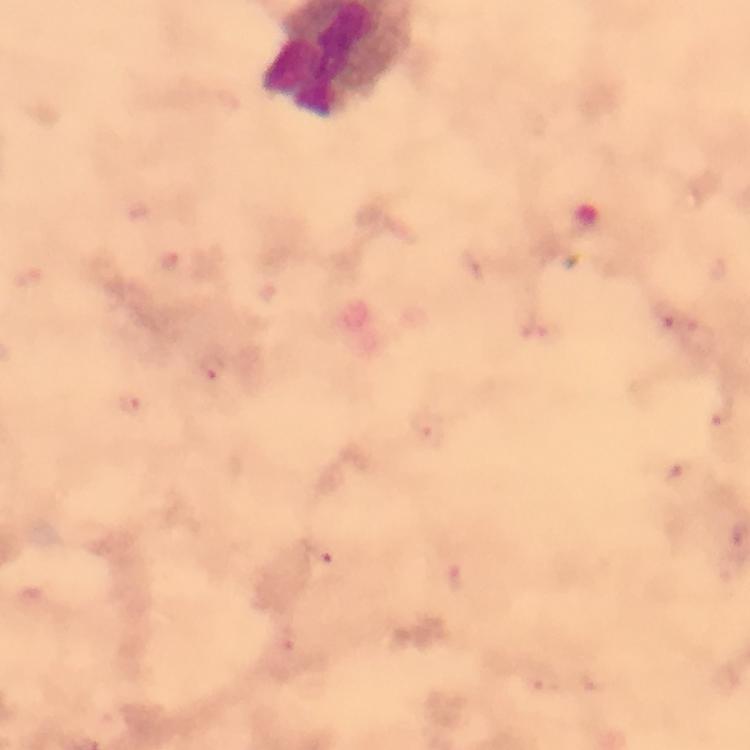
Approximate centers as {x, y} in pixels.
Summary:
  - Plasmodium parasite locations: {666, 317}, {214, 370}, {131, 403}, {322, 556}, {291, 638}
  - Context: from a diagnostic examination for malaria
  - Magnification: 100x
  - Image size: 750×750 pixels
  - Stain: Giemsa
  - Immersion oil: applied
  - Cropped from: one field of view
  - Preparation: thick blood smear
  - Capture: smartphone photograph through a microscope